Identify the parasite.
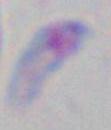
Toxoplasma gondii.

magnification: 1000x
modality: photomicrograph